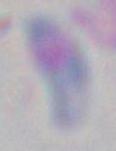

Summary:
  - Magnification: 1000x
  - Modality: photomicrograph
  - Identification: Toxoplasma gondii